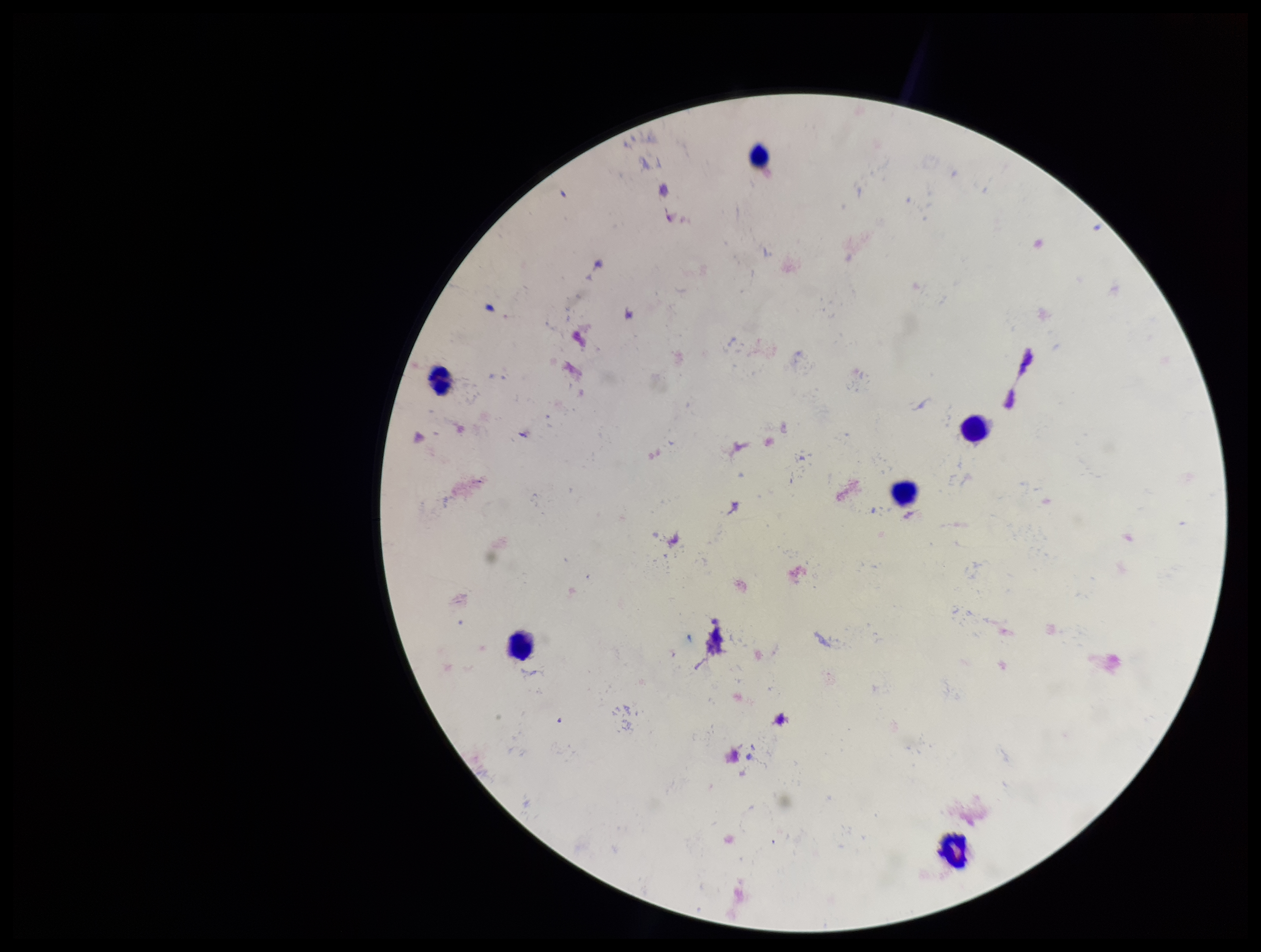
preparation = thick smear
Plasmodium parasites = none detected
parasite count = 0
stain = Giemsa
leukocyte count = 6
capture = smartphone photograph through the microscope eyepiece
image size = 1261×952 pixels
field of view = single
patient malaria status = negative